Locate and identify every blood parasite.
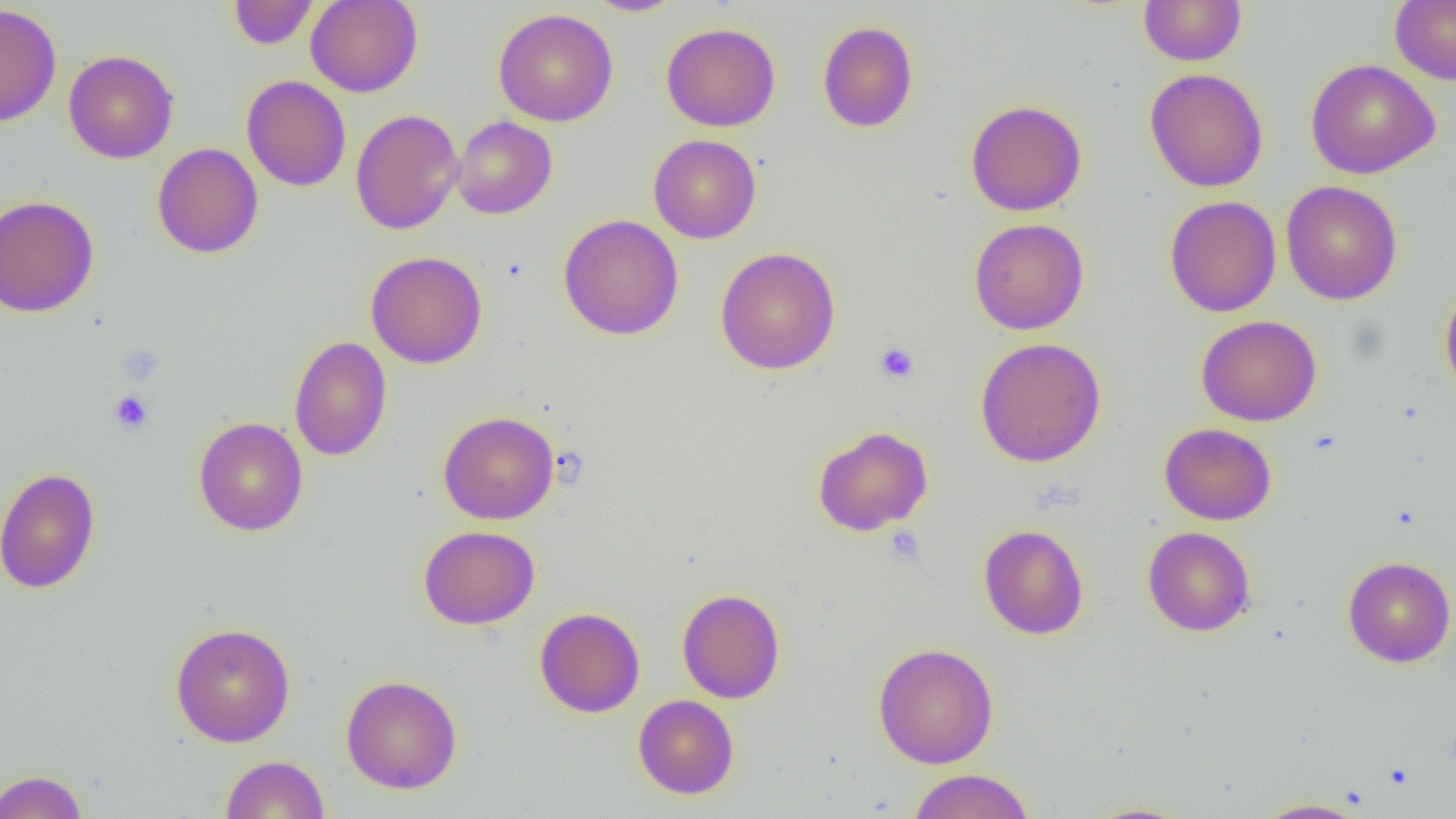

No blood parasites seen.

Summary:
  - Coordinate format: approximate bounding boxes as [x1, y1, x2, y2] in pixels
  - Platelet locations: [874, 342, 919, 384], [109, 391, 153, 434], [883, 526, 926, 566]
  - Uninfected red blood cell locations: [228, 0, 318, 49], [306, 0, 423, 97], [584, 0, 686, 16], [1138, 0, 1247, 66], [1389, 0, 1456, 85], [0, 3, 62, 127], [493, 8, 618, 126], [817, 21, 919, 133], [661, 22, 781, 132], [63, 49, 179, 164], [1305, 58, 1441, 179], [1144, 68, 1269, 192], [241, 74, 351, 191], [965, 100, 1087, 216], [350, 109, 464, 235], [451, 115, 557, 219], [648, 134, 762, 243], [152, 142, 264, 258], [1281, 181, 1403, 305], [0, 195, 99, 317], [1164, 195, 1281, 317], [558, 214, 684, 340], [969, 218, 1089, 335], [715, 246, 841, 374], [366, 250, 488, 369], [1439, 279, 1456, 400], [1196, 315, 1322, 426], [289, 336, 391, 462], [975, 337, 1106, 467], [438, 411, 559, 524], [194, 416, 308, 536], [1159, 423, 1277, 525], [812, 425, 933, 536], [0, 467, 101, 594], [978, 523, 1089, 640], [418, 525, 540, 630], [1143, 526, 1256, 636], [1342, 556, 1456, 668], [677, 588, 785, 703], [534, 607, 645, 717], [170, 622, 296, 747], [873, 642, 999, 768], [341, 674, 463, 794], [633, 694, 739, 798], [220, 755, 330, 818], [907, 768, 1035, 819], [0, 769, 89, 819], [1250, 797, 1370, 818], [1078, 801, 1199, 819]
  - Slide-level diagnosis: negative for blood parasites
  - Preparation: thin blood film
  - Modality: optical microscopy
  - Image size: 1456×819 pixels
  - Field of view: one of a larger specimen
  - Magnification: 1000x